Locate every blood parasite and identify its species.
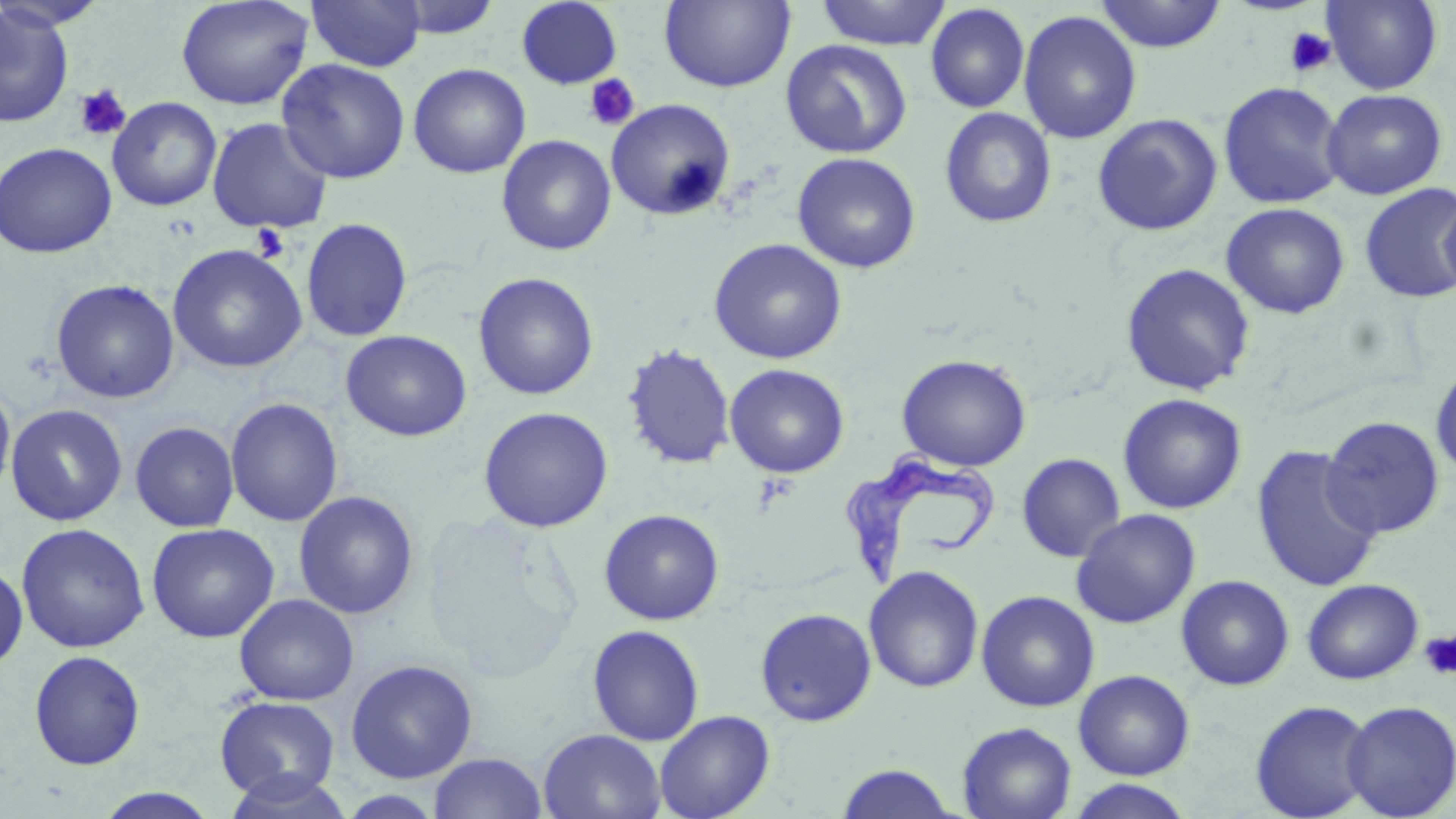
Approximate bounding boxes as named x1/y1/x2/y2 corners in pixels.
Trypanosoma brucei: (x1=840, y1=443, x2=998, y2=590).
No Plasmodium falciparum, Plasmodium ovale, Plasmodium malariae, Plasmodium vivax, or Babesia divergens observed.

Uninfected red blood cell locations: (x1=1, y1=0, x2=111, y2=31), (x1=176, y1=0, x2=314, y2=110), (x1=306, y1=0, x2=426, y2=72), (x1=385, y1=0, x2=505, y2=40), (x1=515, y1=0, x2=624, y2=89), (x1=815, y1=0, x2=951, y2=50), (x1=1094, y1=0, x2=1228, y2=52), (x1=1321, y1=0, x2=1443, y2=94), (x1=659, y1=1, x2=796, y2=93), (x1=925, y1=4, x2=1030, y2=113), (x1=0, y1=5, x2=75, y2=127), (x1=1018, y1=11, x2=1142, y2=144), (x1=780, y1=39, x2=912, y2=159), (x1=276, y1=58, x2=411, y2=184), (x1=408, y1=63, x2=531, y2=178), (x1=1218, y1=81, x2=1346, y2=209), (x1=1321, y1=88, x2=1448, y2=200), (x1=107, y1=97, x2=222, y2=212), (x1=605, y1=98, x2=736, y2=221), (x1=939, y1=107, x2=1057, y2=229), (x1=1092, y1=113, x2=1223, y2=236), (x1=206, y1=117, x2=334, y2=234), (x1=496, y1=134, x2=616, y2=256), (x1=0, y1=142, x2=117, y2=258), (x1=792, y1=152, x2=921, y2=274), (x1=1359, y1=183, x2=1456, y2=304), (x1=1438, y1=191, x2=1456, y2=304), (x1=1221, y1=202, x2=1350, y2=319), (x1=301, y1=217, x2=413, y2=343), (x1=709, y1=238, x2=847, y2=364), (x1=167, y1=244, x2=307, y2=373), (x1=1120, y1=263, x2=1256, y2=396), (x1=473, y1=272, x2=599, y2=401), (x1=50, y1=279, x2=180, y2=404), (x1=341, y1=329, x2=472, y2=442), (x1=622, y1=344, x2=736, y2=470), (x1=896, y1=354, x2=1032, y2=471), (x1=725, y1=363, x2=849, y2=478), (x1=1430, y1=363, x2=1456, y2=479), (x1=0, y1=383, x2=16, y2=502), (x1=1118, y1=393, x2=1247, y2=514), (x1=225, y1=397, x2=343, y2=527), (x1=5, y1=404, x2=128, y2=526), (x1=478, y1=406, x2=614, y2=532), (x1=1320, y1=415, x2=1445, y2=540), (x1=130, y1=421, x2=239, y2=533), (x1=1251, y1=445, x2=1383, y2=592), (x1=1016, y1=453, x2=1126, y2=563), (x1=294, y1=490, x2=419, y2=620), (x1=599, y1=508, x2=725, y2=625), (x1=1071, y1=509, x2=1201, y2=629), (x1=16, y1=523, x2=150, y2=653), (x1=146, y1=523, x2=279, y2=643), (x1=0, y1=561, x2=28, y2=670), (x1=863, y1=565, x2=985, y2=694), (x1=1176, y1=575, x2=1295, y2=691), (x1=1302, y1=578, x2=1423, y2=684), (x1=976, y1=590, x2=1100, y2=712), (x1=234, y1=593, x2=359, y2=706), (x1=755, y1=607, x2=877, y2=726), (x1=587, y1=624, x2=705, y2=746), (x1=29, y1=650, x2=145, y2=771), (x1=345, y1=659, x2=478, y2=783), (x1=1073, y1=669, x2=1196, y2=780), (x1=214, y1=694, x2=340, y2=801), (x1=1249, y1=699, x2=1376, y2=818), (x1=1341, y1=699, x2=1456, y2=818), (x1=654, y1=709, x2=775, y2=819), (x1=957, y1=721, x2=1077, y2=819), (x1=539, y1=728, x2=667, y2=819), (x1=428, y1=753, x2=547, y2=818), (x1=834, y1=763, x2=962, y2=818), (x1=220, y1=771, x2=356, y2=818), (x1=1066, y1=778, x2=1194, y2=819), (x1=94, y1=788, x2=223, y2=818), (x1=336, y1=790, x2=446, y2=818). Platelet locations: (x1=1284, y1=27, x2=1337, y2=78), (x1=583, y1=73, x2=641, y2=132), (x1=74, y1=85, x2=132, y2=141), (x1=251, y1=224, x2=290, y2=262), (x1=1418, y1=630, x2=1456, y2=680). Slide-level diagnosis: Trypanosoma brucei. Captured at 1000x magnification. Thin blood smear. Optical microscopy. Image is 1456×819 pixels. Single field of view. May-Grünwald-Giemsa stain.